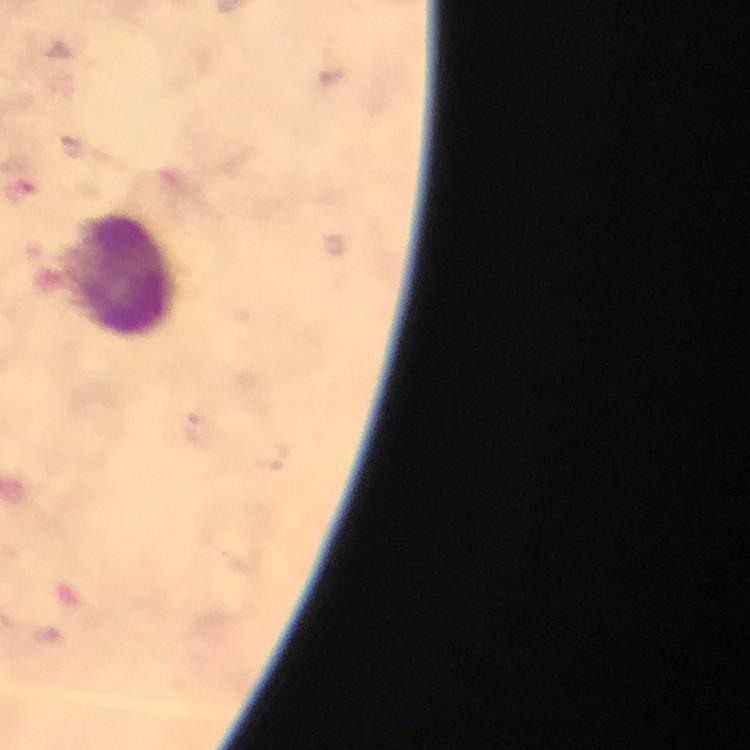
preparation = thick blood smear
immersion oil = used
magnification = 100x
leukocyte locations = approximate centers as {x, y} in pixels: {119, 275}
context = from a malaria diagnostic workup
image size = 750×750 pixels
cropped from = a single field of view
stain = Giemsa
capture = smartphone camera through the microscope
Plasmodium parasite locations = approximate centers as {x, y} in pixels: {72, 145}